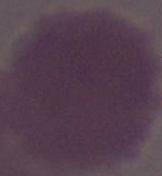

modality = photomicrograph
identification = erythrocyte
magnification = 1000x